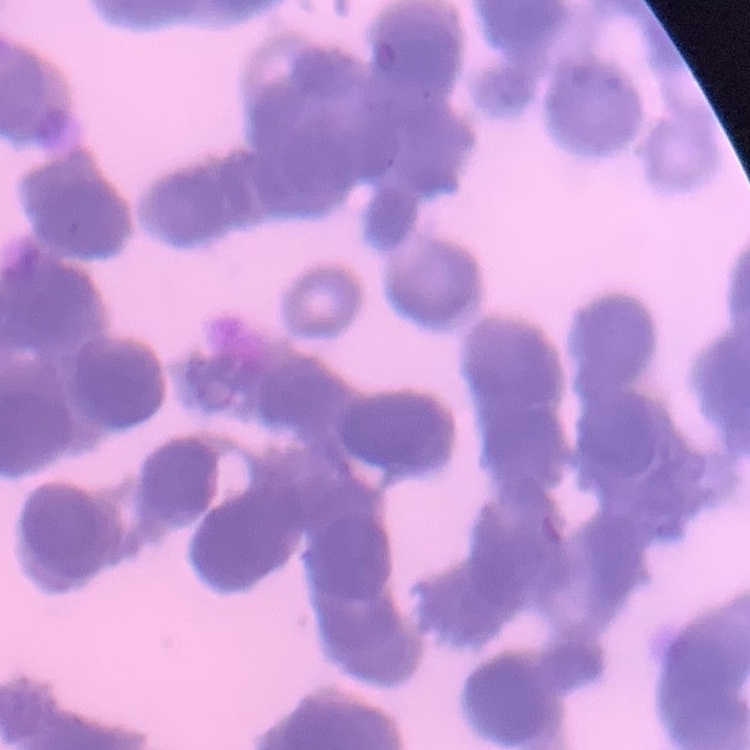

Summary:
  - Erythrocyte morphology: rouleaux formation
  - Preparation: thin peripheral smear
  - Stain: Field's or Giemsa
  - Image type: one tile cut from a larger photomicrograph